Describe the morphology of the erythrocytes.
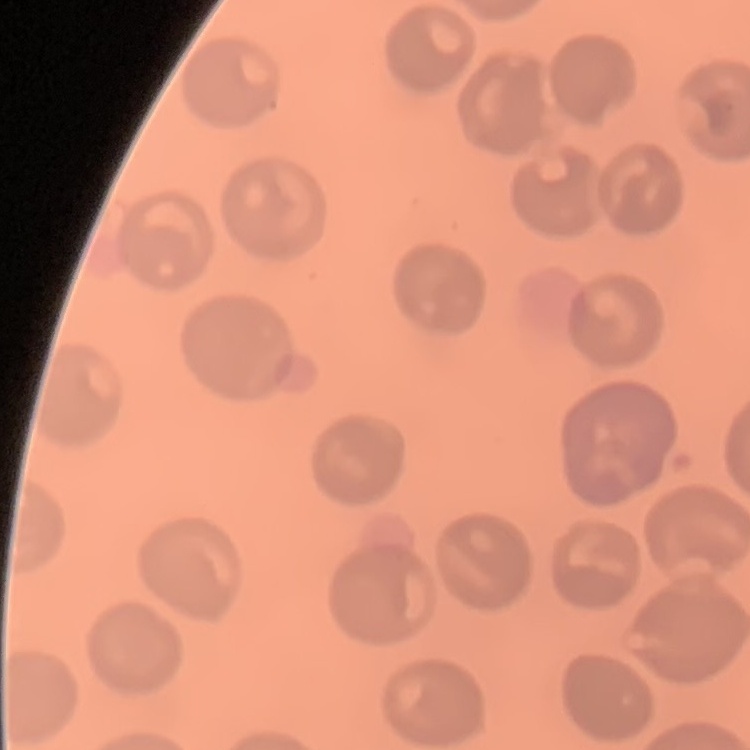

They show no rouleaux formation.

Thin blood film. Square crop of a larger photomicrograph. Stained with either Field's or Giemsa.